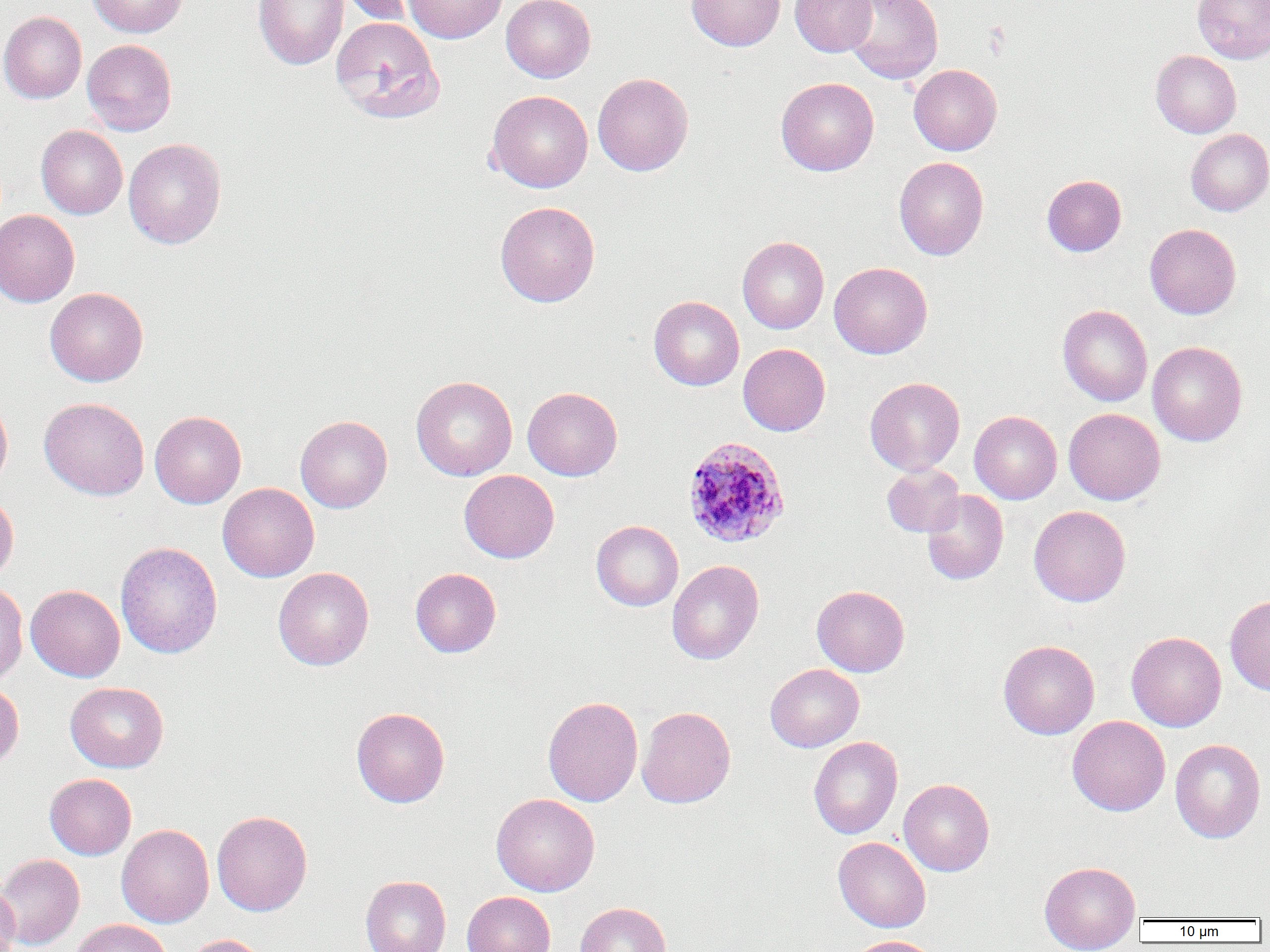

Approximate bounding boxes as (x1, y1, x2, y2) in pixels. Plasmodium ovale-infected red blood cell locations: (682, 436, 790, 548). Uninfected red blood cell locations: (87, 0, 187, 38), (253, 0, 349, 70), (337, 0, 423, 25), (404, 0, 507, 43), (501, 0, 596, 82), (686, 0, 785, 51), (790, 0, 878, 57), (844, 0, 944, 84), (1192, 0, 1269, 64), (0, 11, 87, 103), (330, 16, 445, 123), (82, 39, 177, 136), (1151, 50, 1241, 138), (908, 64, 1002, 155), (592, 73, 693, 176), (776, 77, 879, 176), (487, 90, 593, 193), (36, 125, 127, 219), (1185, 129, 1270, 216), (123, 138, 226, 249), (894, 156, 988, 260), (1041, 174, 1126, 256), (495, 201, 600, 307), (0, 209, 80, 307), (1144, 223, 1241, 319), (737, 236, 829, 334), (829, 262, 932, 359), (45, 287, 148, 386), (648, 295, 744, 390), (1058, 304, 1152, 406), (1147, 341, 1247, 446), (738, 343, 831, 436), (410, 376, 518, 481), (865, 377, 965, 475), (523, 387, 622, 480), (0, 395, 13, 490), (39, 397, 149, 500), (1063, 408, 1165, 505), (150, 410, 246, 508), (969, 411, 1062, 504), (295, 415, 392, 513), (882, 464, 965, 537), (459, 470, 559, 563), (218, 482, 319, 582), (922, 490, 1008, 585), (0, 493, 19, 585), (1029, 505, 1131, 607), (591, 520, 683, 611), (115, 542, 222, 658), (666, 560, 764, 664), (273, 567, 374, 670), (410, 567, 501, 657), (0, 580, 28, 685), (26, 584, 125, 682), (812, 585, 910, 677), (1225, 594, 1270, 696), (1126, 631, 1226, 731), (998, 639, 1100, 739), (765, 663, 864, 752), (0, 679, 24, 769), (66, 682, 169, 772), (543, 696, 643, 807), (637, 706, 736, 808), (351, 707, 450, 807), (1067, 716, 1170, 816), (1066, 728, 1266, 826), (808, 736, 902, 839), (1170, 739, 1266, 843), (44, 773, 136, 859), (899, 779, 994, 876), (491, 793, 600, 896), (212, 810, 312, 917), (116, 824, 214, 927), (833, 836, 931, 933), (0, 854, 85, 949), (1039, 861, 1141, 951), (360, 875, 451, 952), (0, 881, 20, 952), (462, 891, 556, 952), (575, 902, 672, 952), (69, 919, 173, 952), (182, 934, 269, 952), (844, 935, 941, 952). Slide-level diagnosis: Plasmodium ovale. Thin blood smear. Optical microscopy. 1000x magnification. Image is 1270×952 pixels. Single field of view.